Assess this cell for malaria.
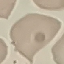

Uninfected.

Summary:
  - Preparation: thin blood film
  - Capture: smartphone camera at the microscope eyepiece
  - Stain: Giemsa
  - Image type: cell patch, automatically extracted from a larger field of view and resized to 64 × 64 pixels